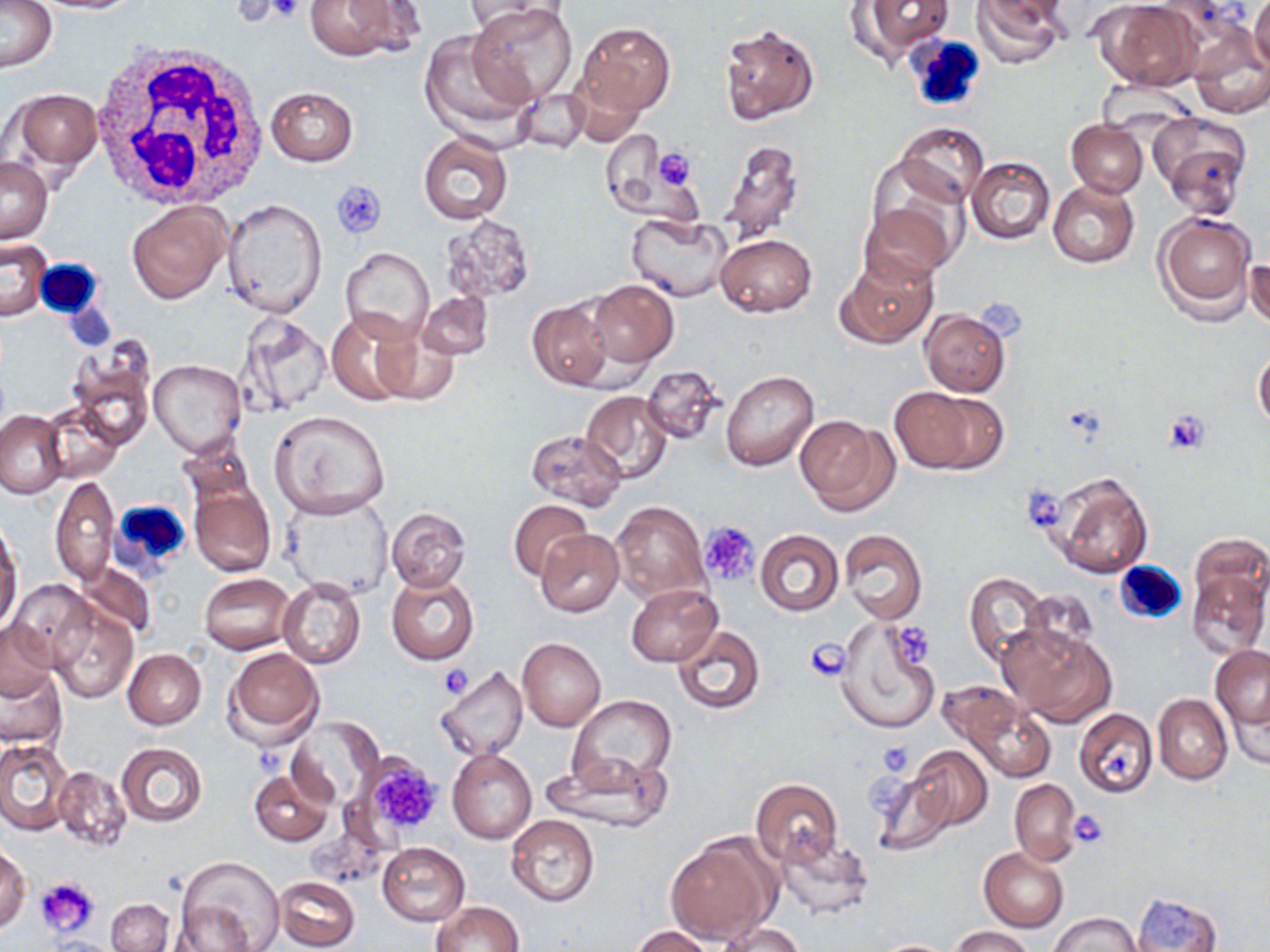
Summary:
  - Coordinate format: approximate bounding boxes as named x1/y1/x2/y2 corners in pixels
  - White blood cell locations: (x1=905, y1=35, x2=986, y2=112), (x1=87, y1=43, x2=270, y2=215), (x1=34, y1=260, x2=105, y2=320), (x1=114, y1=499, x2=196, y2=574), (x1=1114, y1=561, x2=1188, y2=626)
  - Platelet locations: (x1=264, y1=0, x2=306, y2=24), (x1=651, y1=149, x2=698, y2=192), (x1=332, y1=179, x2=387, y2=239), (x1=1164, y1=411, x2=1211, y2=454), (x1=1022, y1=483, x2=1067, y2=533), (x1=699, y1=520, x2=762, y2=587), (x1=888, y1=621, x2=938, y2=669), (x1=805, y1=639, x2=850, y2=682), (x1=439, y1=664, x2=473, y2=699), (x1=877, y1=741, x2=913, y2=777), (x1=361, y1=753, x2=444, y2=837), (x1=1069, y1=810, x2=1109, y2=847), (x1=36, y1=877, x2=101, y2=936)
  - Uninfected red blood cell locations: (x1=0, y1=0, x2=58, y2=73), (x1=22, y1=0, x2=152, y2=14), (x1=303, y1=0, x2=421, y2=62), (x1=464, y1=0, x2=566, y2=37), (x1=852, y1=0, x2=953, y2=60), (x1=970, y1=0, x2=1069, y2=65), (x1=1249, y1=0, x2=1270, y2=75), (x1=1094, y1=2, x2=1204, y2=91), (x1=469, y1=3, x2=576, y2=106), (x1=573, y1=20, x2=675, y2=122), (x1=718, y1=20, x2=821, y2=128), (x1=420, y1=32, x2=531, y2=137), (x1=1189, y1=36, x2=1270, y2=119), (x1=264, y1=86, x2=359, y2=165), (x1=10, y1=88, x2=103, y2=175), (x1=515, y1=88, x2=590, y2=154), (x1=1148, y1=112, x2=1252, y2=216), (x1=1067, y1=119, x2=1147, y2=197), (x1=896, y1=122, x2=988, y2=205), (x1=602, y1=129, x2=668, y2=213), (x1=417, y1=132, x2=513, y2=224), (x1=720, y1=136, x2=805, y2=245), (x1=966, y1=156, x2=1055, y2=245), (x1=0, y1=157, x2=52, y2=243), (x1=863, y1=159, x2=966, y2=260), (x1=1047, y1=180, x2=1140, y2=267), (x1=223, y1=199, x2=326, y2=317), (x1=861, y1=200, x2=957, y2=285), (x1=127, y1=202, x2=231, y2=304), (x1=1154, y1=210, x2=1258, y2=321), (x1=626, y1=212, x2=734, y2=302), (x1=441, y1=215, x2=537, y2=301), (x1=714, y1=234, x2=817, y2=317), (x1=0, y1=239, x2=50, y2=323), (x1=341, y1=246, x2=434, y2=346), (x1=1247, y1=248, x2=1270, y2=335), (x1=835, y1=254, x2=938, y2=349), (x1=586, y1=279, x2=677, y2=368), (x1=417, y1=289, x2=494, y2=361), (x1=527, y1=299, x2=615, y2=391), (x1=324, y1=307, x2=425, y2=406), (x1=920, y1=309, x2=1011, y2=396), (x1=238, y1=312, x2=332, y2=415), (x1=369, y1=319, x2=462, y2=406), (x1=1254, y1=347, x2=1270, y2=430), (x1=68, y1=348, x2=155, y2=448), (x1=148, y1=360, x2=246, y2=458), (x1=641, y1=364, x2=725, y2=444), (x1=721, y1=369, x2=818, y2=471), (x1=890, y1=385, x2=1005, y2=475), (x1=580, y1=390, x2=673, y2=483), (x1=42, y1=404, x2=124, y2=484), (x1=0, y1=409, x2=67, y2=499), (x1=268, y1=410, x2=391, y2=518), (x1=795, y1=414, x2=898, y2=514), (x1=526, y1=429, x2=626, y2=510), (x1=1048, y1=471, x2=1153, y2=577), (x1=50, y1=476, x2=118, y2=584), (x1=188, y1=483, x2=276, y2=578), (x1=280, y1=493, x2=396, y2=603), (x1=509, y1=499, x2=590, y2=581), (x1=612, y1=501, x2=710, y2=601), (x1=386, y1=506, x2=472, y2=594), (x1=0, y1=528, x2=23, y2=636), (x1=839, y1=528, x2=927, y2=624), (x1=534, y1=529, x2=624, y2=617), (x1=755, y1=530, x2=844, y2=616), (x1=1188, y1=533, x2=1269, y2=614), (x1=74, y1=563, x2=156, y2=638), (x1=1186, y1=568, x2=1269, y2=658), (x1=385, y1=572, x2=479, y2=665), (x1=964, y1=572, x2=1051, y2=670), (x1=200, y1=573, x2=295, y2=654), (x1=277, y1=576, x2=365, y2=670), (x1=9, y1=581, x2=95, y2=669), (x1=626, y1=584, x2=719, y2=665), (x1=1023, y1=589, x2=1098, y2=657), (x1=49, y1=607, x2=138, y2=702), (x1=836, y1=619, x2=940, y2=735), (x1=0, y1=620, x2=59, y2=698), (x1=1001, y1=621, x2=1117, y2=727), (x1=672, y1=625, x2=767, y2=714), (x1=517, y1=637, x2=606, y2=732), (x1=223, y1=647, x2=325, y2=747), (x1=1211, y1=647, x2=1270, y2=731), (x1=122, y1=649, x2=206, y2=729), (x1=435, y1=664, x2=528, y2=762), (x1=1, y1=666, x2=66, y2=749), (x1=1223, y1=678, x2=1269, y2=771), (x1=935, y1=681, x2=1027, y2=750), (x1=568, y1=694, x2=678, y2=788), (x1=1153, y1=694, x2=1232, y2=784), (x1=963, y1=697, x2=1057, y2=783), (x1=1073, y1=708, x2=1158, y2=798), (x1=289, y1=718, x2=382, y2=807), (x1=0, y1=739, x2=71, y2=834), (x1=118, y1=742, x2=207, y2=827), (x1=897, y1=745, x2=993, y2=839), (x1=447, y1=749, x2=537, y2=845), (x1=544, y1=750, x2=672, y2=834), (x1=54, y1=766, x2=131, y2=851), (x1=248, y1=767, x2=333, y2=846), (x1=750, y1=779, x2=842, y2=867), (x1=1009, y1=779, x2=1080, y2=865), (x1=1069, y1=806, x2=1110, y2=858), (x1=505, y1=814, x2=599, y2=907), (x1=772, y1=832, x2=874, y2=918), (x1=665, y1=834, x2=779, y2=944), (x1=376, y1=842, x2=470, y2=926), (x1=0, y1=845, x2=31, y2=933), (x1=979, y1=847, x2=1069, y2=933), (x1=175, y1=856, x2=286, y2=952), (x1=275, y1=875, x2=360, y2=951), (x1=1129, y1=892, x2=1224, y2=951), (x1=107, y1=899, x2=173, y2=952), (x1=431, y1=901, x2=524, y2=952), (x1=169, y1=902, x2=258, y2=949), (x1=1048, y1=911, x2=1142, y2=951), (x1=713, y1=921, x2=807, y2=951), (x1=630, y1=925, x2=714, y2=952), (x1=948, y1=926, x2=1037, y2=952), (x1=43, y1=935, x2=123, y2=952), (x1=866, y1=938, x2=963, y2=951)
  - Slide-level diagnosis: no evidence of blood parasites
  - Magnification: 1000x
  - Field of view: one of a larger specimen
  - Preparation: thin blood film
  - Stain: May-Grünwald-Giemsa
  - Image size: 1270×952 pixels
  - Modality: optical microscopy